Describe the morphology of the red blood cells.
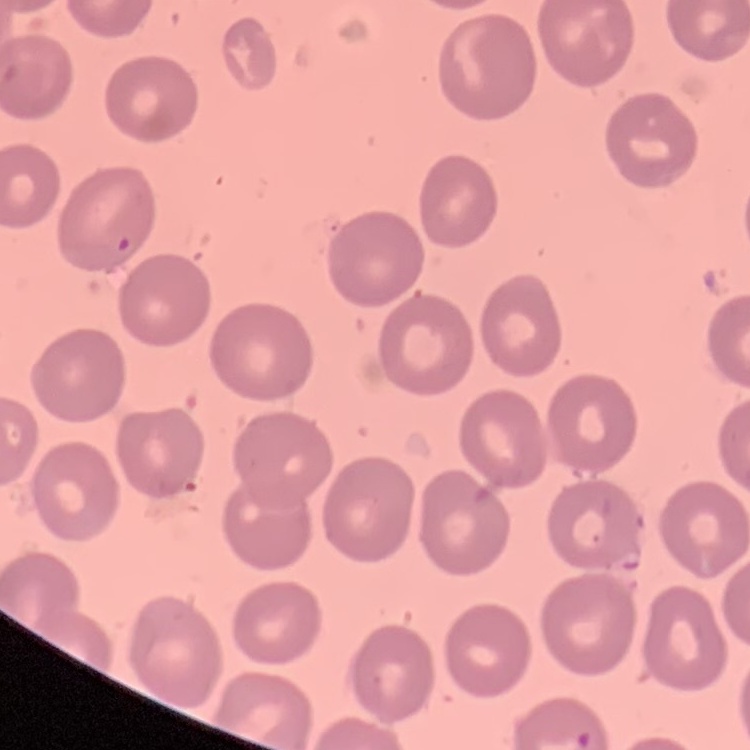

No rouleaux formation.

Field's or Giemsa stain. Thin blood film. Square crop of a larger photomicrograph.